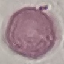
Summary:
  - Malaria status: uninfected
  - Image type: cell patch, automatically extracted from a larger field of view and resized to 64 × 64 pixels
  - Capture: smartphone camera at the microscope eyepiece
  - Preparation: thin blood smear
  - Stain: Giemsa